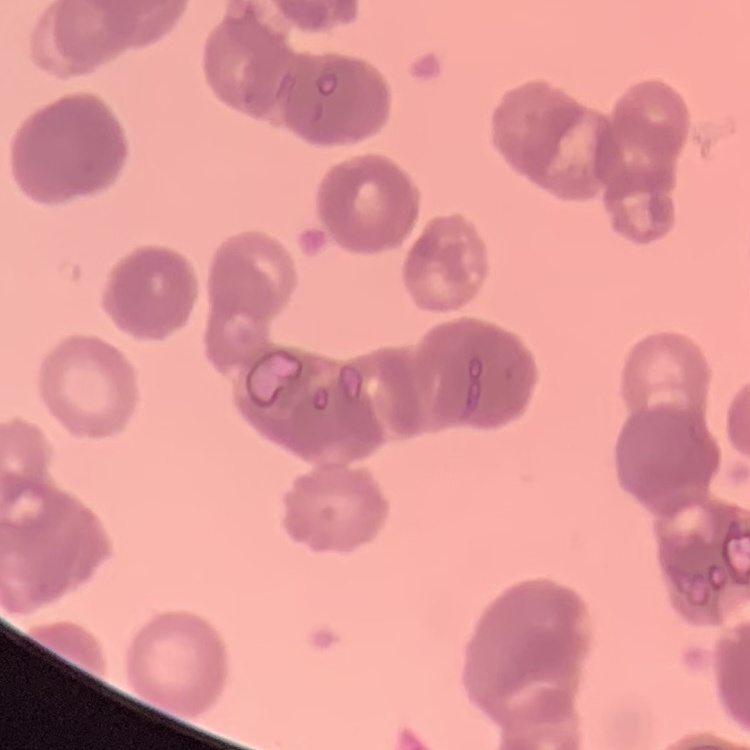

The erythrocytes show rouleaux formation. Stained with either Field's or Giemsa. Square crop of a larger photomicrograph. Thin blood film.